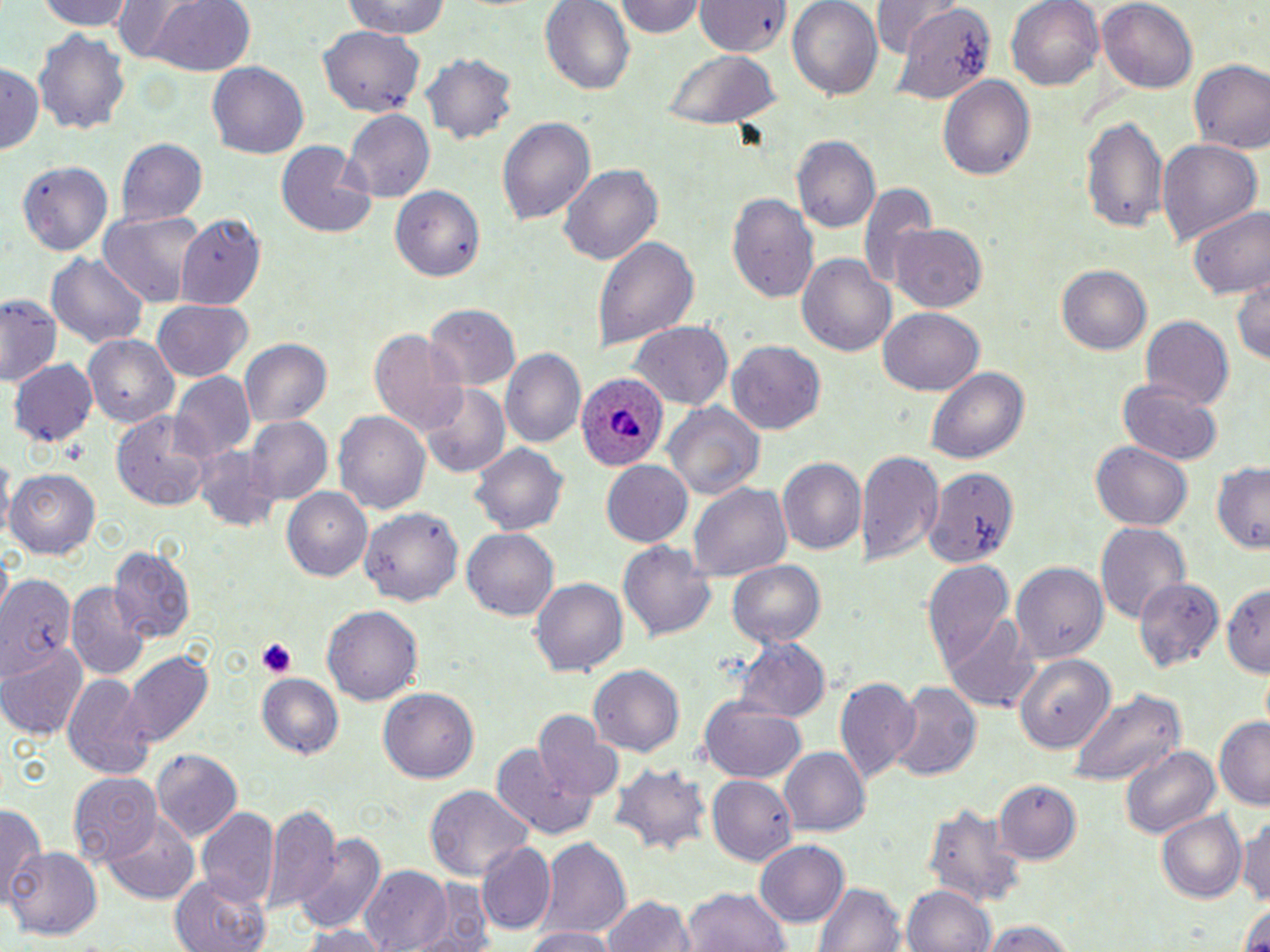 Approximate bounding boxes as (x1,y1)-(x2,y2) corner pairs in pixels. Uninfected red blood cell locations: (37,0)-(136,30), (141,0)-(258,77), (615,0)-(709,40), (692,0)-(792,58), (786,0)-(882,98), (871,0)-(956,57), (1006,0)-(1103,92), (1098,0)-(1198,90), (338,1)-(454,41), (540,1)-(635,94), (892,5)-(996,103), (319,27)-(426,113), (33,32)-(130,133), (663,48)-(778,129), (421,52)-(518,145), (1189,60)-(1270,155), (0,62)-(43,157), (206,62)-(309,159), (938,75)-(1036,180), (342,110)-(434,202), (1080,113)-(1168,233), (499,115)-(595,228), (792,136)-(879,236), (116,138)-(207,226), (274,140)-(376,239), (1157,140)-(1262,242), (16,159)-(114,256), (560,164)-(660,266), (859,184)-(939,290), (392,187)-(485,282), (727,189)-(818,303), (1189,204)-(1269,301), (98,210)-(208,306), (175,216)-(267,308), (890,224)-(987,312), (593,235)-(697,353), (44,254)-(150,349), (799,254)-(895,358), (1057,264)-(1151,356), (1231,270)-(1270,366), (1,294)-(61,385), (152,298)-(252,381), (423,302)-(520,392), (878,305)-(984,394), (1139,317)-(1233,410), (630,323)-(731,409), (369,329)-(471,438), (85,335)-(177,426), (237,335)-(334,428), (729,341)-(825,436), (502,348)-(584,448), (10,359)-(97,449), (927,366)-(1030,466), (170,374)-(255,461), (1119,380)-(1223,466), (420,383)-(510,478), (664,403)-(766,500), (111,409)-(218,510), (333,409)-(431,516), (246,417)-(332,505), (1091,441)-(1194,532), (470,443)-(567,538), (193,445)-(281,531), (858,448)-(941,567), (776,457)-(865,558), (600,460)-(692,547), (1210,463)-(1270,552), (923,466)-(1018,572), (8,468)-(100,560), (688,482)-(792,583), (281,488)-(371,582), (361,505)-(465,607), (1095,521)-(1189,625), (462,529)-(559,622), (618,539)-(717,642), (108,546)-(194,645), (729,558)-(826,648), (922,558)-(1015,673), (1011,562)-(1110,662), (1,576)-(77,674), (530,578)-(626,680), (1136,578)-(1221,672), (1223,579)-(1270,679), (67,583)-(150,682), (324,606)-(422,705), (945,613)-(1037,712), (732,636)-(831,725), (0,645)-(88,741), (123,651)-(213,745), (1014,654)-(1118,751), (589,664)-(685,758), (62,671)-(154,781), (833,675)-(917,781), (257,676)-(343,759), (888,682)-(981,782), (1067,685)-(1187,784), (381,687)-(481,782), (699,702)-(806,783), (534,713)-(622,803), (1214,718)-(1270,807), (1118,742)-(1221,842), (494,747)-(603,841), (777,747)-(869,837), (150,748)-(243,838), (612,765)-(710,856), (68,772)-(163,864), (707,775)-(797,863), (995,779)-(1081,863), (424,787)-(531,883), (921,798)-(1028,912), (263,802)-(345,912), (1,804)-(44,909), (197,808)-(278,912), (1155,809)-(1247,904), (104,813)-(200,902), (1240,813)-(1270,911), (293,832)-(388,935), (536,837)-(632,938), (474,840)-(558,935), (754,840)-(848,927), (8,847)-(102,942), (359,865)-(456,951), (169,874)-(272,952), (409,879)-(496,952), (813,881)-(908,952), (685,885)-(791,952), (901,885)-(996,952), (1235,893)-(1270,952), (601,894)-(696,952), (978,922)-(1078,952), (292,924)-(395,952), (521,925)-(619,952). Platelet locations: (256,637)-(298,680). Plasmodium ovale-infected red blood cell locations: (579,370)-(669,471). Slide-level diagnosis: Plasmodium ovale. 1000x magnification. Light microscopy. Single field of view. May-Grünwald-Giemsa-stained preparation. Image is 1270×952 pixels. Thin blood smear.